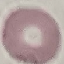
Result: negative for malaria parasites. Photographed with a smartphone camera at the microscope eyepiece. Cell patch, automatically extracted from a larger field of view and resized to 64 × 64 pixels. Giemsa stain. Thin blood film.